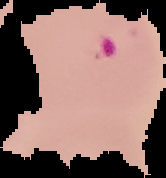
Result: Plasmodium parasites identified. Cell region segmented out of the field of view; the surrounding area is masked to black. From a thin blood film. Image is 166×178 pixels.